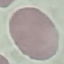
result = no malaria parasites detected
preparation = thin blood smear
capture = smartphone through the microscope eyepiece
stain = Giemsa
image type = automatically extracted cell patch, resized to 64 × 64 pixels